Name the parasite shown.
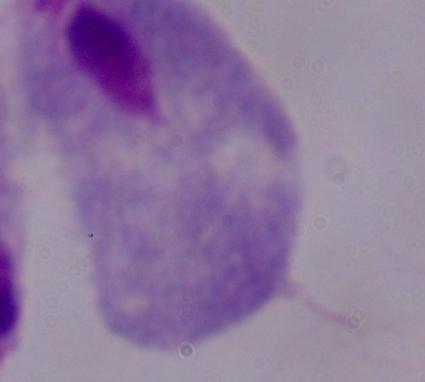
This is a trichomonad.

Summary:
  - Modality: photomicrograph
  - Magnification: 1000x